Outline every Plasmodium parasite.
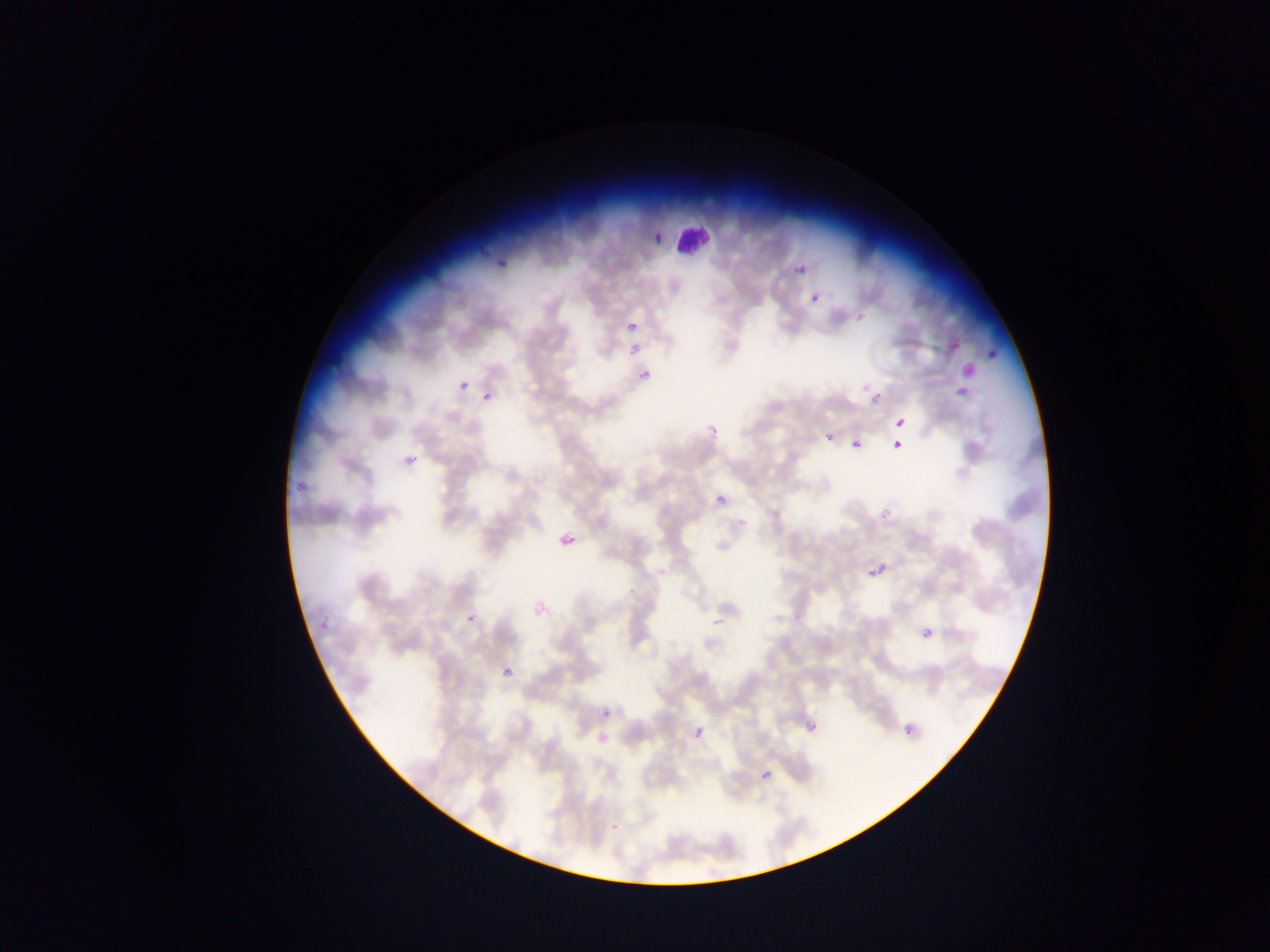
Approximate bounding boxes as (left, top, right, bottom) in pixels.
Plasmodium parasites: (646, 226, 661, 247), (791, 255, 808, 273), (494, 256, 515, 264), (811, 293, 822, 304), (852, 308, 866, 323), (628, 319, 642, 334), (946, 339, 961, 351), (985, 345, 1002, 363), (637, 367, 657, 381), (456, 379, 471, 391), (482, 391, 493, 403), (869, 395, 881, 407), (894, 417, 907, 430), (705, 420, 724, 441), (826, 433, 835, 442), (892, 439, 905, 452), (852, 440, 861, 450), (401, 446, 418, 467), (293, 479, 305, 492), (717, 495, 727, 505), (876, 501, 890, 519), (737, 517, 751, 532), (557, 528, 580, 554), (865, 561, 888, 583), (317, 610, 328, 629), (464, 611, 481, 631), (709, 615, 726, 622), (918, 623, 940, 647), (501, 665, 517, 682), (602, 709, 612, 719), (805, 717, 817, 731), (900, 721, 919, 742), (695, 728, 705, 739), (597, 732, 609, 746), (757, 767, 776, 788), (610, 822, 621, 834).

Summary:
  - Leukocyte locations: (669, 220, 715, 258)
  - Field of view: single
  - Capture: mobile-phone photograph through a microscope
  - Preparation: thin blood smear
  - Image size: 1270×952 pixels
  - Country: Ghana